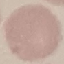
Malaria status: uninfected. Giemsa stain. Automatically extracted cell patch, resized to 64 × 64 pixels. Photographed with a smartphone camera at the microscope eyepiece. Thin blood film.